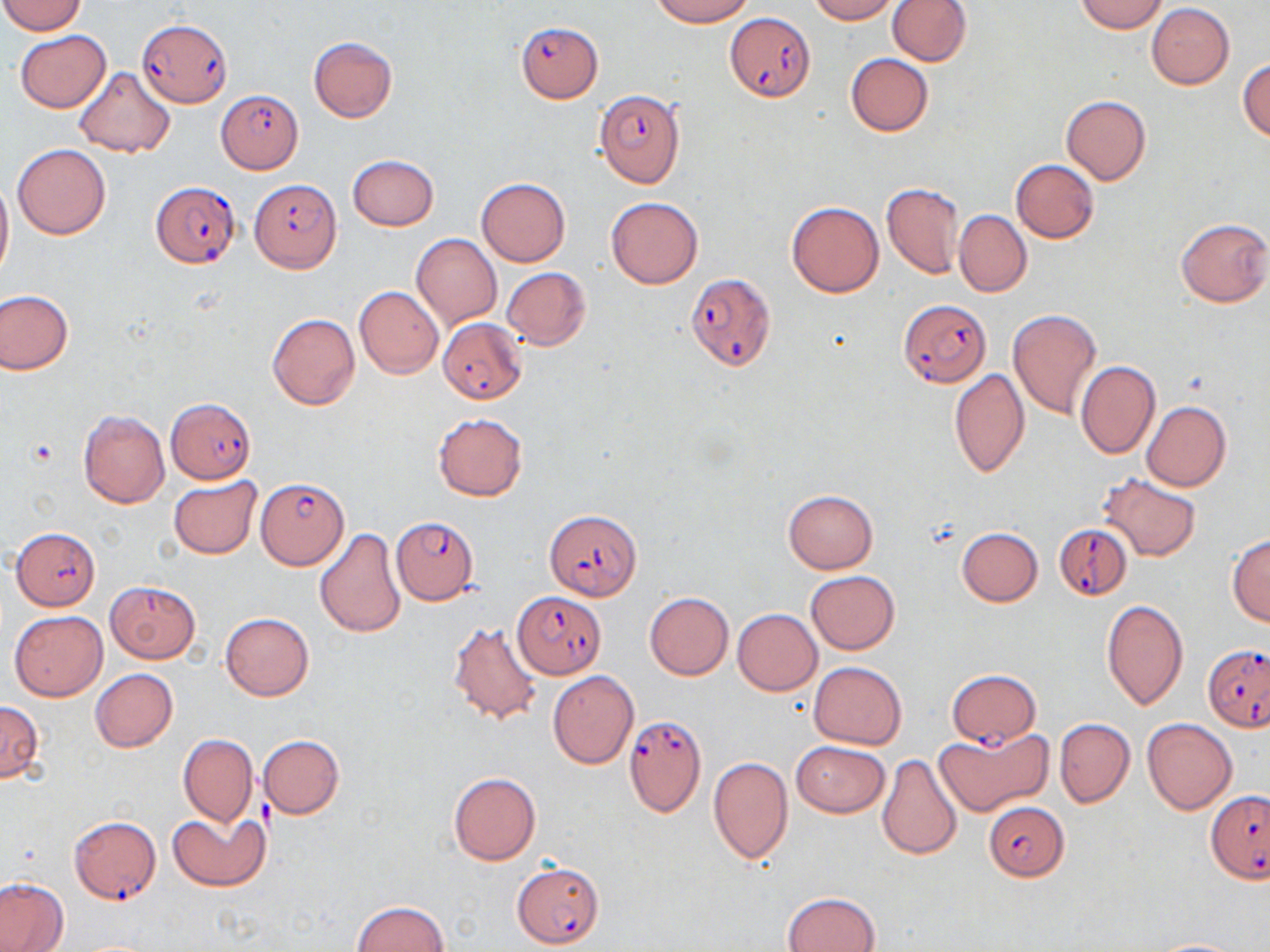 Approximate bounding boxes as [x1, y1, x2, y2] in pixels. Uninfected red blood cell locations: [652, 0, 753, 26], [807, 0, 897, 23], [886, 0, 972, 65], [1076, 0, 1168, 33], [0, 1, 87, 35], [1147, 2, 1234, 89], [15, 30, 111, 113], [308, 36, 397, 121], [844, 52, 934, 135], [1238, 58, 1269, 142], [73, 68, 175, 158], [1060, 95, 1152, 185], [12, 144, 111, 239], [348, 154, 439, 230], [1010, 159, 1099, 242], [0, 171, 13, 281], [477, 178, 570, 266], [880, 181, 964, 279], [606, 197, 704, 289], [786, 201, 884, 297], [954, 211, 1031, 296], [1175, 217, 1270, 308], [411, 234, 502, 329], [502, 267, 591, 350], [355, 286, 443, 378], [0, 289, 73, 374], [1007, 308, 1102, 419], [267, 313, 360, 410], [1076, 360, 1160, 458], [950, 368, 1030, 479], [1141, 401, 1231, 492], [78, 409, 169, 508], [433, 412, 527, 501], [1097, 472, 1203, 563], [168, 476, 262, 559], [782, 490, 879, 573], [956, 527, 1043, 607], [314, 528, 407, 637], [1227, 533, 1270, 627], [806, 570, 900, 656], [104, 581, 201, 663], [644, 592, 734, 680], [1101, 600, 1188, 710], [733, 608, 822, 694], [10, 611, 107, 701], [220, 611, 314, 700], [448, 619, 544, 725], [809, 661, 907, 749], [90, 669, 178, 753], [547, 670, 639, 768], [0, 699, 45, 782], [1141, 717, 1238, 814], [1054, 718, 1135, 807], [936, 726, 1050, 818], [179, 734, 257, 826], [258, 735, 345, 818], [792, 741, 890, 817], [876, 753, 964, 860], [708, 757, 793, 865], [447, 773, 541, 865], [167, 812, 268, 892], [0, 878, 70, 951], [782, 891, 882, 952], [350, 900, 450, 952], [1145, 938, 1252, 951]. Plasmodium falciparum-infected red blood cell locations: [725, 13, 815, 102], [137, 20, 233, 105], [516, 22, 602, 102], [216, 89, 304, 174], [594, 89, 685, 188], [250, 179, 343, 272], [151, 180, 240, 268], [684, 271, 776, 371], [898, 299, 990, 385], [439, 317, 526, 403], [168, 400, 255, 481], [256, 476, 347, 570], [543, 509, 643, 600], [393, 517, 478, 602], [1053, 521, 1132, 599], [10, 527, 101, 609], [514, 592, 604, 676], [1203, 644, 1268, 730], [948, 669, 1041, 746], [623, 716, 708, 817], [1206, 791, 1270, 881], [986, 800, 1071, 881], [69, 815, 161, 904], [513, 862, 604, 948]. Platelet locations: [27, 437, 60, 468]. Slide-level diagnosis: Plasmodium falciparum. Image is 1270×952 pixels. Thin blood smear. May-Grünwald-Giemsa stain. 1000x magnification. Optical microscopy. Single field of view.